Outline each uninfected red blood cell.
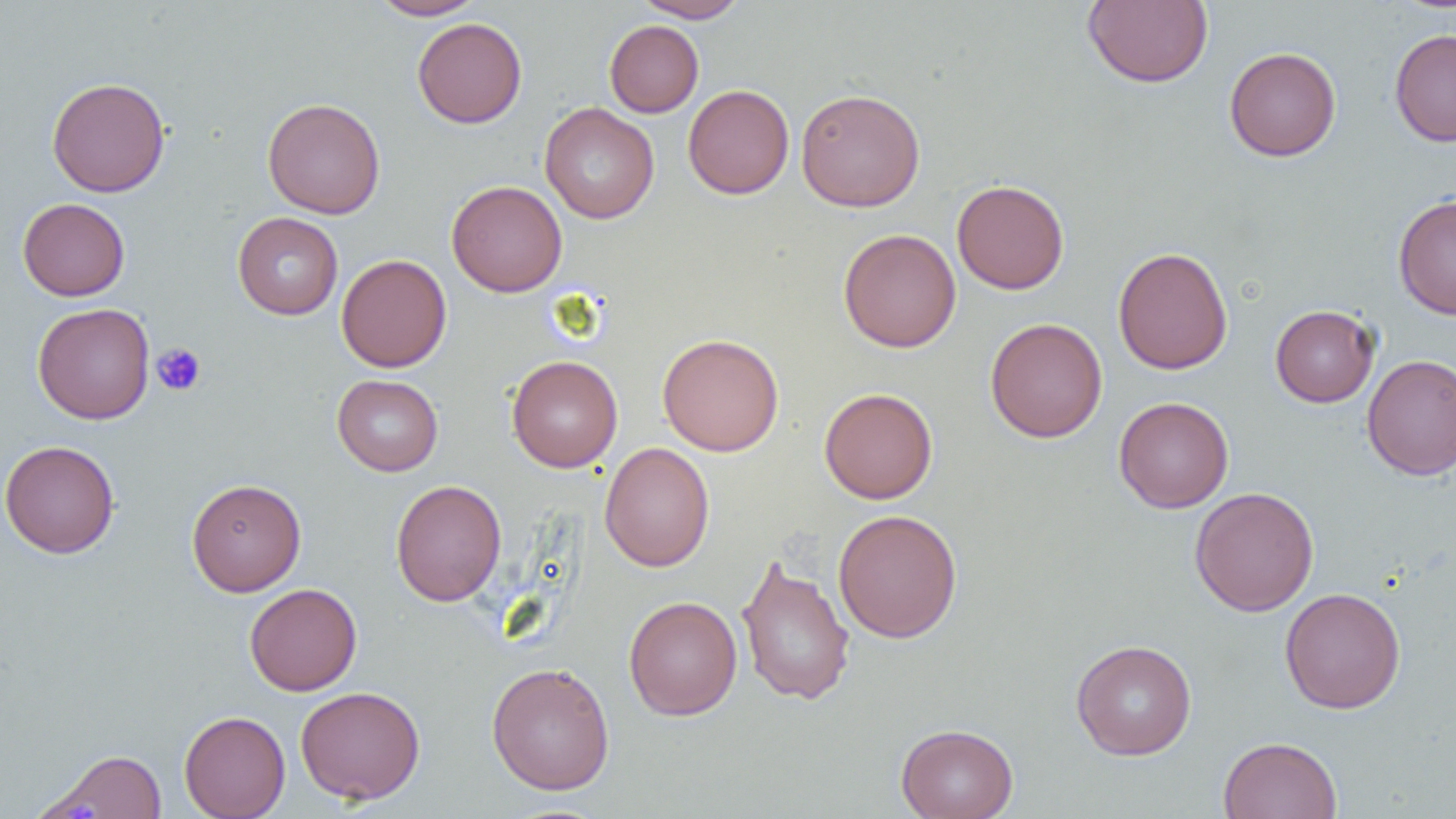
Approximate bounding boxes as (x1, y1, x2, y2) in pixels.
Uninfected red blood cells: (369, 0, 485, 20), (632, 0, 750, 23), (1082, 0, 1214, 89), (412, 17, 527, 128), (604, 19, 704, 118), (1389, 27, 1456, 147), (1224, 46, 1342, 161), (47, 77, 170, 197), (683, 84, 794, 199), (795, 88, 925, 212), (262, 97, 386, 219), (539, 102, 659, 224), (951, 179, 1069, 295), (446, 180, 567, 297), (1393, 194, 1456, 319), (17, 198, 130, 301), (232, 212, 344, 320), (838, 228, 961, 353), (1113, 246, 1233, 375), (336, 254, 452, 372), (33, 302, 155, 425), (1270, 304, 1380, 407), (985, 317, 1108, 443), (657, 333, 784, 456), (1362, 353, 1456, 481), (506, 355, 623, 472), (332, 374, 443, 476), (818, 387, 938, 504), (1113, 396, 1234, 513), (0, 440, 120, 559), (599, 442, 715, 572), (186, 478, 306, 596), (390, 480, 507, 607), (1189, 486, 1319, 616), (833, 509, 963, 644), (736, 553, 856, 706), (244, 583, 362, 696), (1279, 587, 1406, 713), (623, 595, 742, 721), (1070, 639, 1198, 760), (486, 662, 615, 795), (295, 686, 425, 804), (179, 710, 290, 819), (895, 723, 1018, 819), (1218, 736, 1342, 819), (38, 748, 169, 818).

{
  "slide_level_diagnosis": "no evidence of blood parasites",
  "preparation": "thin blood film",
  "magnification": "1000x",
  "field_of_view": "one of a larger specimen",
  "modality": "light microscopy",
  "platelet_locations": "approximate bounding boxes as (x1, y1, x2, y2) in pixels: (151, 343, 206, 396)",
  "image_size": "1456×819 pixels"
}